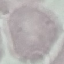

{
  "malaria_status": "uninfected",
  "preparation": "thin blood smear",
  "stain": "Giemsa",
  "capture": "smartphone through the microscope eyepiece",
  "image_type": "cell patch, automatically extracted from a larger field of view and resized to 64 × 64 pixels"
}